Assess this cell for malaria.
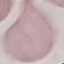

Uninfected.

Giemsa-stained preparation. Acquired by smartphone through the microscope eyepiece. Thin smear of blood. Cell patch, automatically extracted from a larger field of view and resized to 64 × 64 pixels.